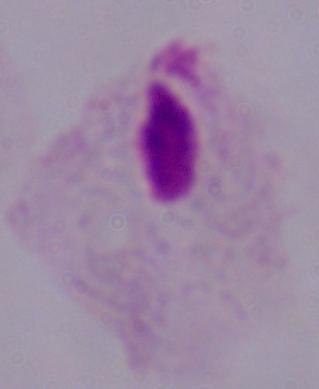
1000x magnification. A trichomonad is seen. Photomicrograph.